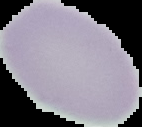

preparation = thin blood smear
result = no malaria parasites detected
image size = 142×127 pixels
image type = segmented cell region on a black background